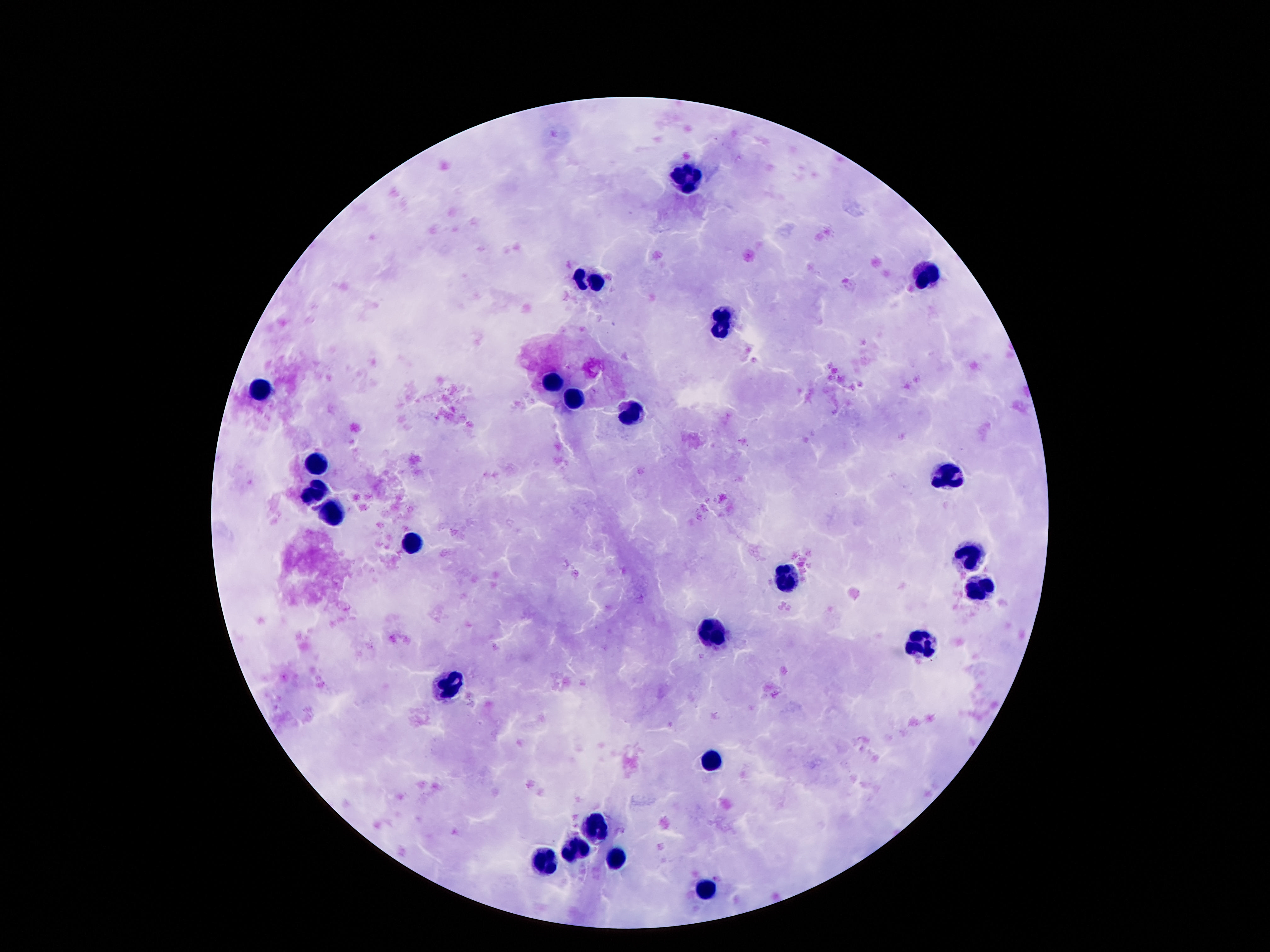
Approximate object centers, in pixels from the top-left corner. Leukocyte locations: (x=687, y=180), (x=925, y=275), (x=591, y=278), (x=724, y=325), (x=548, y=383), (x=259, y=387), (x=578, y=399), (x=630, y=414), (x=316, y=462), (x=951, y=473), (x=316, y=493), (x=335, y=516), (x=414, y=544), (x=972, y=553), (x=787, y=577), (x=978, y=587), (x=716, y=633), (x=922, y=646), (x=449, y=682), (x=713, y=763), (x=597, y=829), (x=576, y=847), (x=545, y=863), (x=617, y=863), (x=705, y=890). 100x magnification. Patient malaria status: negative. Thick blood smear. Giemsa stain. Single field of view. Image is 1270×952 pixels. Smartphone photograph taken through the microscope eyepiece.